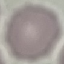

malaria status = uninfected
capture = smartphone camera at the microscope eyepiece
stain = Giemsa
image type = cell patch, automatically extracted from a larger field of view and resized to 64 × 64 pixels
preparation = thin smear